Identify the cell.
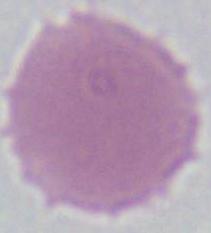
An erythrocyte.

Summary:
  - Modality: micrograph
  - Magnification: 1000x